Locate every uninfected red blood cell.
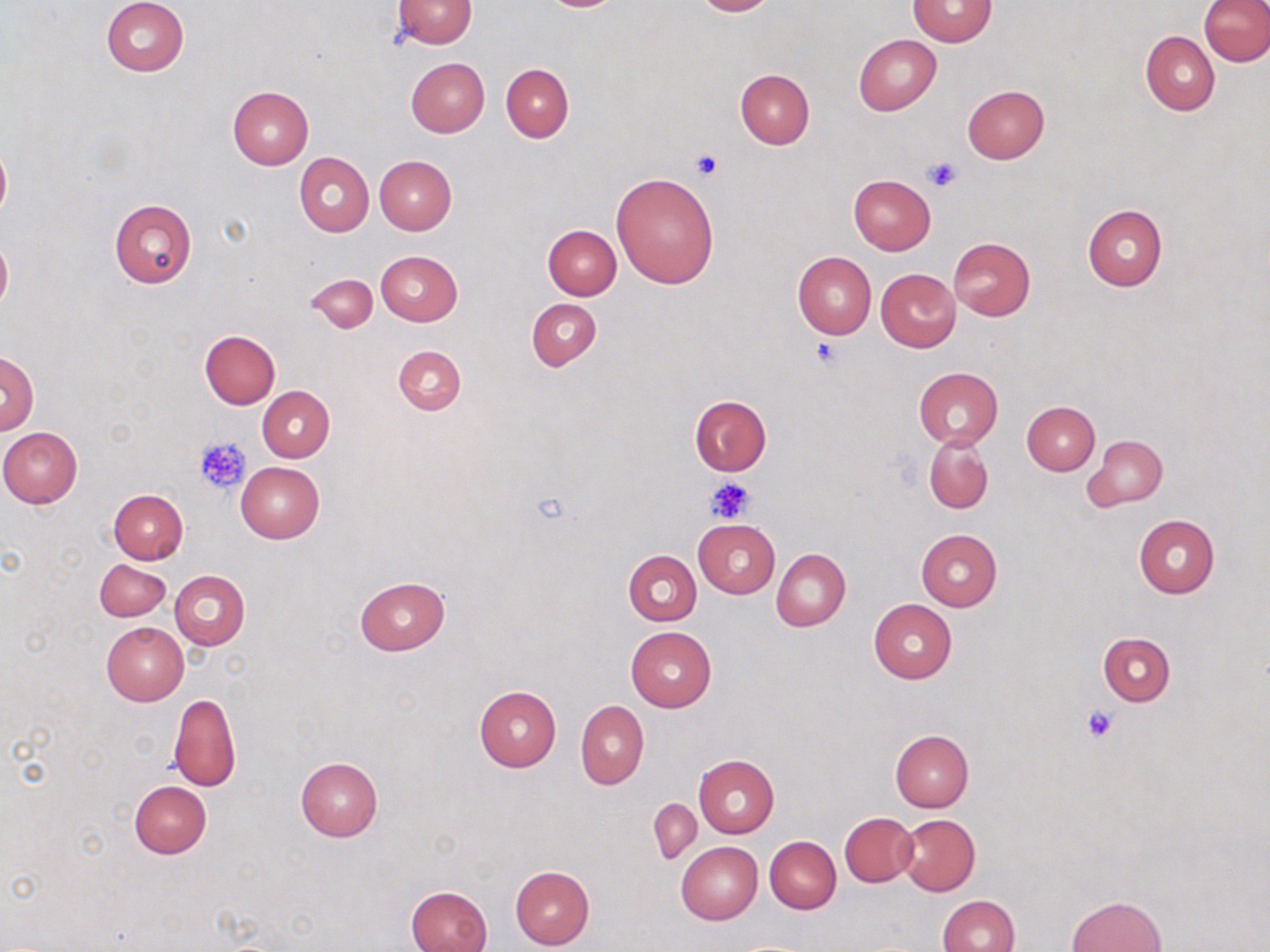
Approximate bounding boxes as (x1, y1, x2, y2) in pixels.
Uninfected red blood cells: (101, 0, 188, 76), (392, 0, 478, 48), (690, 0, 778, 16), (909, 1, 997, 46), (1201, 1, 1270, 66), (1141, 30, 1220, 115), (853, 34, 942, 115), (405, 57, 489, 138), (501, 63, 573, 142), (734, 69, 815, 148), (962, 84, 1049, 163), (227, 85, 314, 168), (1, 143, 11, 219), (294, 152, 374, 236), (375, 155, 456, 235), (611, 172, 719, 288), (849, 175, 936, 254), (109, 200, 196, 287), (1082, 205, 1166, 291), (543, 224, 622, 299), (0, 236, 12, 311), (947, 237, 1035, 320), (375, 250, 462, 326), (793, 251, 877, 339), (876, 269, 960, 352), (306, 274, 377, 334), (526, 298, 600, 371), (200, 331, 280, 408), (393, 345, 466, 414), (0, 350, 38, 434), (913, 367, 1002, 449), (258, 386, 335, 462), (689, 396, 771, 475), (1021, 401, 1099, 475), (0, 428, 83, 508), (924, 434, 994, 514), (1085, 435, 1167, 510), (236, 462, 325, 543), (108, 490, 187, 564), (1133, 514, 1219, 598), (693, 519, 779, 598), (916, 528, 1002, 611), (771, 549, 851, 631), (623, 551, 701, 626), (95, 559, 170, 621), (170, 570, 250, 649), (354, 577, 449, 654), (868, 599, 957, 683), (102, 622, 188, 705), (625, 627, 716, 713), (1098, 632, 1175, 706), (475, 685, 561, 771), (169, 694, 242, 793), (576, 700, 649, 790), (891, 730, 973, 812), (694, 754, 779, 839), (294, 756, 383, 842), (129, 782, 211, 858), (649, 798, 701, 864), (838, 812, 918, 888), (896, 814, 981, 896), (765, 836, 841, 913), (675, 841, 763, 924), (509, 864, 594, 950), (406, 885, 491, 952), (937, 895, 1019, 952), (1066, 895, 1167, 951).

Platelet locations: (689, 150, 723, 181), (923, 156, 960, 193), (812, 337, 846, 369), (196, 437, 249, 494), (706, 477, 754, 524), (1083, 705, 1121, 743). Slide-level diagnosis: negative for blood parasites. May-Grünwald-Giemsa stain. Thin blood smear. 1000x magnification. Image is 1270×952 pixels. Optical microscopy. One field of a larger specimen.